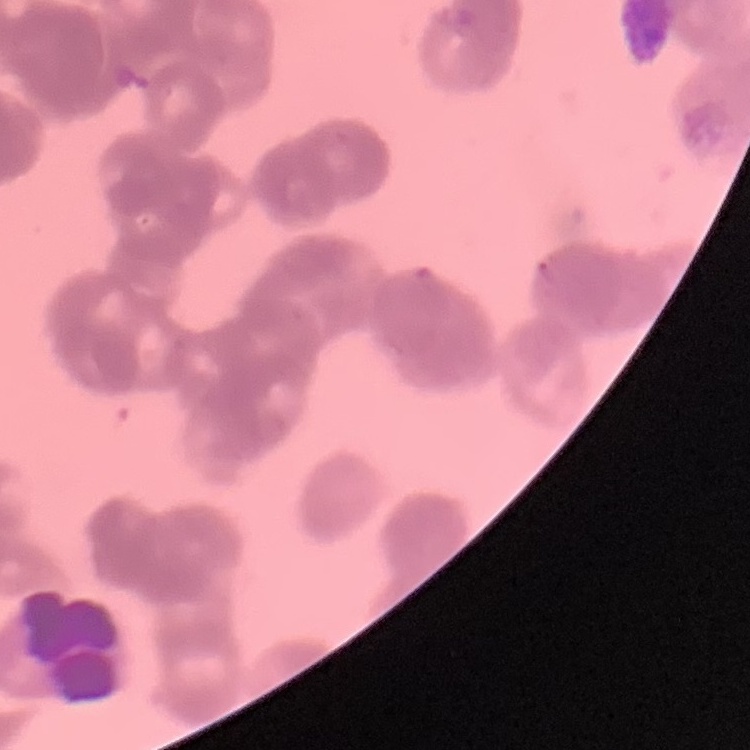
{
  "erythrocyte_morphology": "rouleaux formation",
  "image_type": "one tile cut from a larger photomicrograph",
  "stain": "Field's or Giemsa",
  "preparation": "thin blood smear"
}